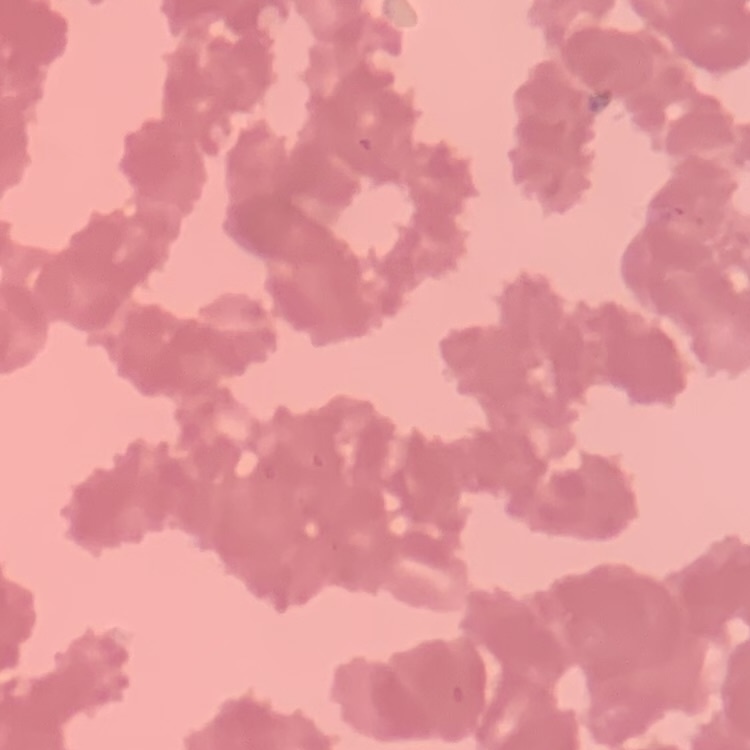

{
  "erythrocyte_morphology": "rouleaux formation",
  "image_type": "square crop of a larger photomicrograph",
  "stain": "Field's or Giemsa",
  "preparation": "thin blood smear"
}